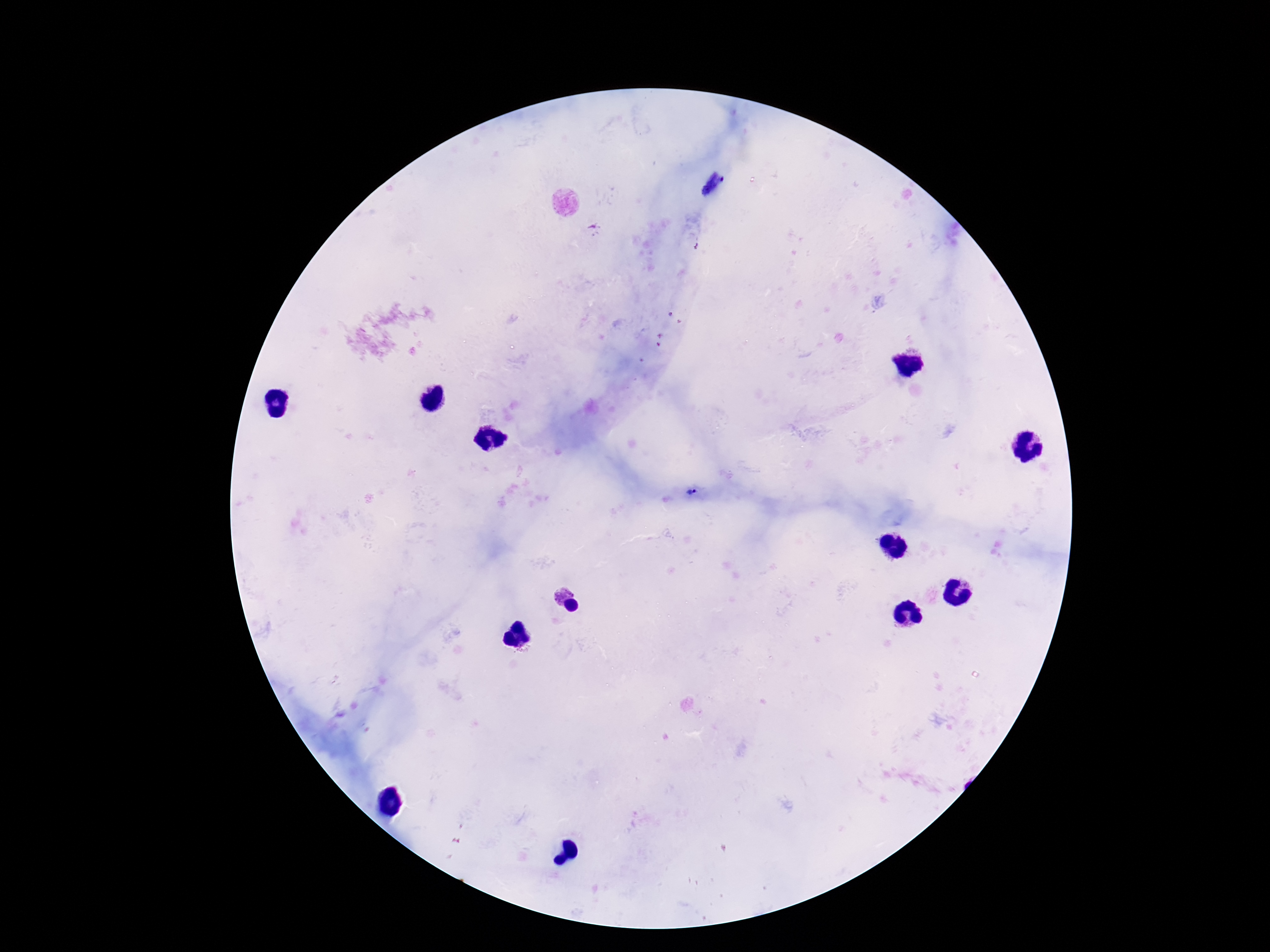
stain: Giemsa
capture: smartphone camera through the microscope eyepiece
field_of_view: one from this slide
image_size: 1270×952 pixels
magnification: 100x
patient_malaria_status: positive
plasmodium_parasite_locations: 'approximate centers as (x, y) in pixels: (691, 493)'
preparation: thick peripheral-blood smear